Locate and identify every blood parasite.
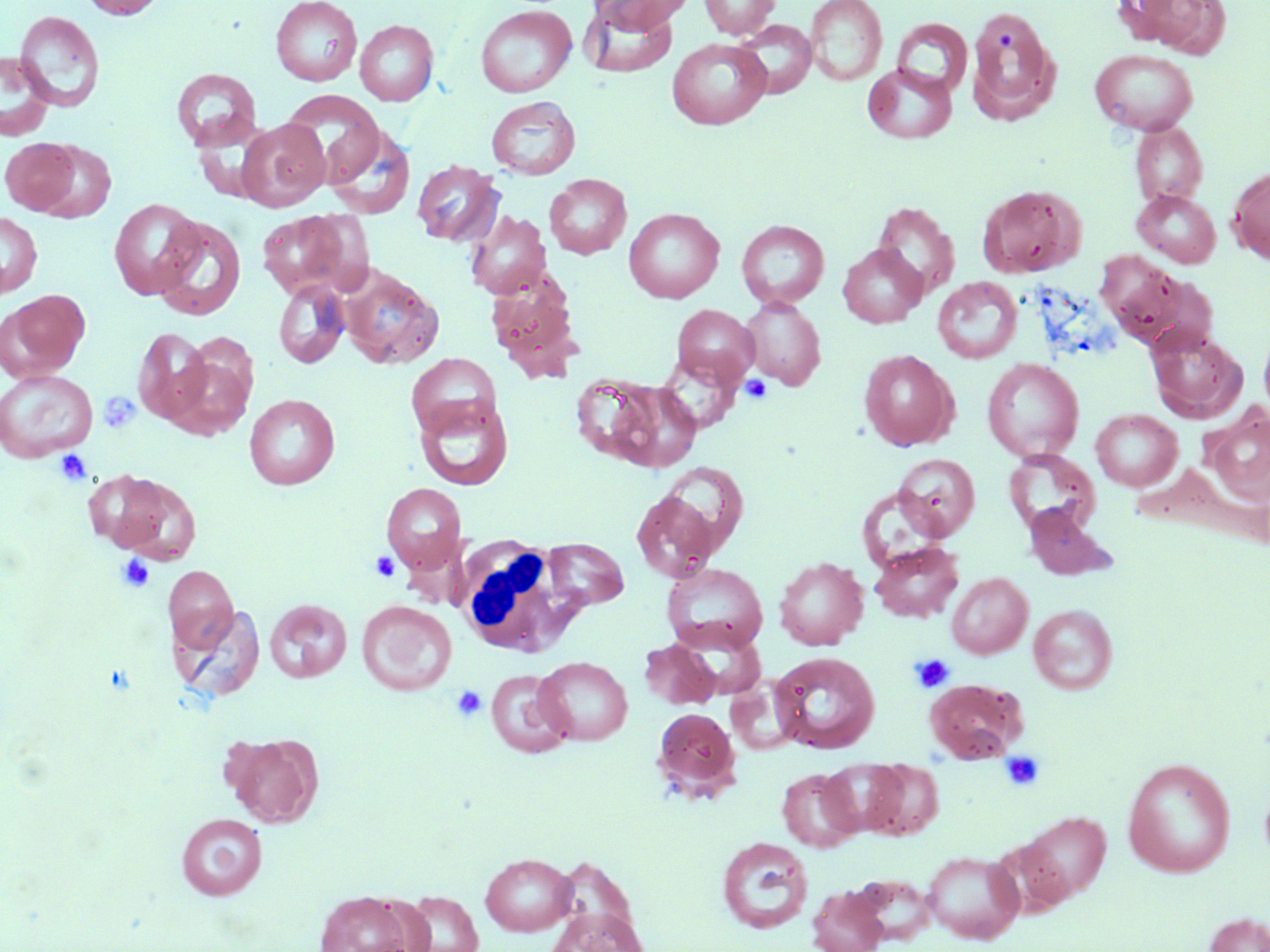
No blood parasites seen.

Approximate bounding boxes as named x1/y1/x2/y2 corners in pixels. Platelet locations: (x1=740, y1=375, x2=772, y2=404), (x1=99, y1=390, x2=137, y2=435), (x1=54, y1=449, x2=92, y2=486), (x1=370, y1=551, x2=400, y2=582), (x1=115, y1=553, x2=156, y2=594), (x1=911, y1=653, x2=954, y2=693), (x1=451, y1=686, x2=487, y2=722), (x1=1000, y1=750, x2=1046, y2=791). White blood cell locations: (x1=456, y1=537, x2=588, y2=657). Uninfected red blood cell locations: (x1=79, y1=0, x2=167, y2=19), (x1=270, y1=0, x2=362, y2=86), (x1=590, y1=0, x2=693, y2=32), (x1=698, y1=0, x2=781, y2=38), (x1=805, y1=0, x2=888, y2=86), (x1=1125, y1=0, x2=1230, y2=58), (x1=580, y1=3, x2=678, y2=79), (x1=474, y1=4, x2=577, y2=98), (x1=965, y1=4, x2=1062, y2=126), (x1=14, y1=10, x2=105, y2=112), (x1=892, y1=18, x2=972, y2=97), (x1=355, y1=20, x2=438, y2=105), (x1=734, y1=20, x2=817, y2=98), (x1=667, y1=39, x2=771, y2=130), (x1=1089, y1=49, x2=1198, y2=135), (x1=0, y1=51, x2=54, y2=141), (x1=862, y1=63, x2=957, y2=144), (x1=171, y1=68, x2=262, y2=152), (x1=280, y1=90, x2=384, y2=186), (x1=486, y1=96, x2=580, y2=179), (x1=236, y1=119, x2=329, y2=211), (x1=1130, y1=122, x2=1208, y2=207), (x1=325, y1=124, x2=415, y2=219), (x1=1, y1=137, x2=80, y2=214), (x1=33, y1=140, x2=116, y2=223), (x1=411, y1=159, x2=504, y2=246), (x1=1228, y1=166, x2=1270, y2=264), (x1=544, y1=174, x2=631, y2=259), (x1=977, y1=184, x2=1086, y2=278), (x1=1133, y1=190, x2=1221, y2=267), (x1=109, y1=197, x2=202, y2=299), (x1=872, y1=202, x2=960, y2=297), (x1=624, y1=208, x2=724, y2=303), (x1=256, y1=210, x2=364, y2=299), (x1=466, y1=210, x2=552, y2=299), (x1=0, y1=212, x2=42, y2=297), (x1=152, y1=215, x2=246, y2=320), (x1=737, y1=219, x2=829, y2=308), (x1=838, y1=244, x2=927, y2=328), (x1=1094, y1=251, x2=1210, y2=352), (x1=340, y1=266, x2=444, y2=369), (x1=485, y1=271, x2=583, y2=381), (x1=931, y1=277, x2=1022, y2=363), (x1=274, y1=279, x2=351, y2=369), (x1=1, y1=290, x2=90, y2=382), (x1=740, y1=298, x2=826, y2=390), (x1=672, y1=304, x2=759, y2=385), (x1=1258, y1=325, x2=1270, y2=418), (x1=1145, y1=326, x2=1248, y2=423), (x1=133, y1=327, x2=212, y2=424), (x1=164, y1=347, x2=255, y2=439), (x1=859, y1=349, x2=959, y2=451), (x1=656, y1=351, x2=744, y2=435), (x1=406, y1=353, x2=501, y2=439), (x1=982, y1=358, x2=1084, y2=462), (x1=0, y1=368, x2=98, y2=462), (x1=570, y1=373, x2=668, y2=467), (x1=604, y1=381, x2=703, y2=471), (x1=244, y1=393, x2=339, y2=489), (x1=415, y1=394, x2=514, y2=490), (x1=1204, y1=407, x2=1270, y2=505), (x1=1091, y1=408, x2=1183, y2=491), (x1=1004, y1=449, x2=1100, y2=536), (x1=893, y1=453, x2=980, y2=540), (x1=658, y1=461, x2=749, y2=556), (x1=99, y1=472, x2=203, y2=563), (x1=380, y1=483, x2=466, y2=573), (x1=631, y1=490, x2=719, y2=582), (x1=1024, y1=506, x2=1114, y2=581), (x1=542, y1=538, x2=628, y2=610), (x1=869, y1=541, x2=964, y2=622), (x1=773, y1=556, x2=868, y2=650), (x1=661, y1=562, x2=768, y2=654), (x1=163, y1=565, x2=238, y2=653), (x1=947, y1=572, x2=1033, y2=659), (x1=265, y1=598, x2=352, y2=683), (x1=356, y1=601, x2=457, y2=696), (x1=173, y1=602, x2=266, y2=705), (x1=1028, y1=604, x2=1117, y2=694), (x1=639, y1=639, x2=720, y2=709), (x1=770, y1=651, x2=881, y2=753), (x1=535, y1=656, x2=633, y2=745), (x1=485, y1=669, x2=574, y2=758), (x1=924, y1=679, x2=1027, y2=762), (x1=652, y1=707, x2=740, y2=800), (x1=225, y1=733, x2=323, y2=828), (x1=822, y1=758, x2=908, y2=835), (x1=1122, y1=758, x2=1235, y2=877), (x1=861, y1=760, x2=943, y2=839), (x1=777, y1=767, x2=862, y2=852), (x1=1015, y1=810, x2=1111, y2=905), (x1=176, y1=813, x2=267, y2=900), (x1=716, y1=836, x2=813, y2=934), (x1=921, y1=850, x2=1025, y2=943), (x1=480, y1=852, x2=577, y2=936), (x1=807, y1=885, x2=889, y2=952), (x1=314, y1=891, x2=417, y2=952), (x1=400, y1=891, x2=483, y2=952), (x1=545, y1=905, x2=648, y2=952), (x1=1204, y1=912, x2=1270, y2=952). Slide-level diagnosis: no evidence of blood parasites. Thin blood film. Optical microscopy. Image is 1270×952 pixels. Captured at 1000x magnification. May-Grünwald-Giemsa-stained preparation. Single field of view.